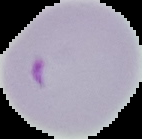
Summary:
  - Image size: 142×139 pixels
  - Image type: segmented cell region with the area outside set to black
  - Malaria status: parasitized
  - Preparation: thin blood smear